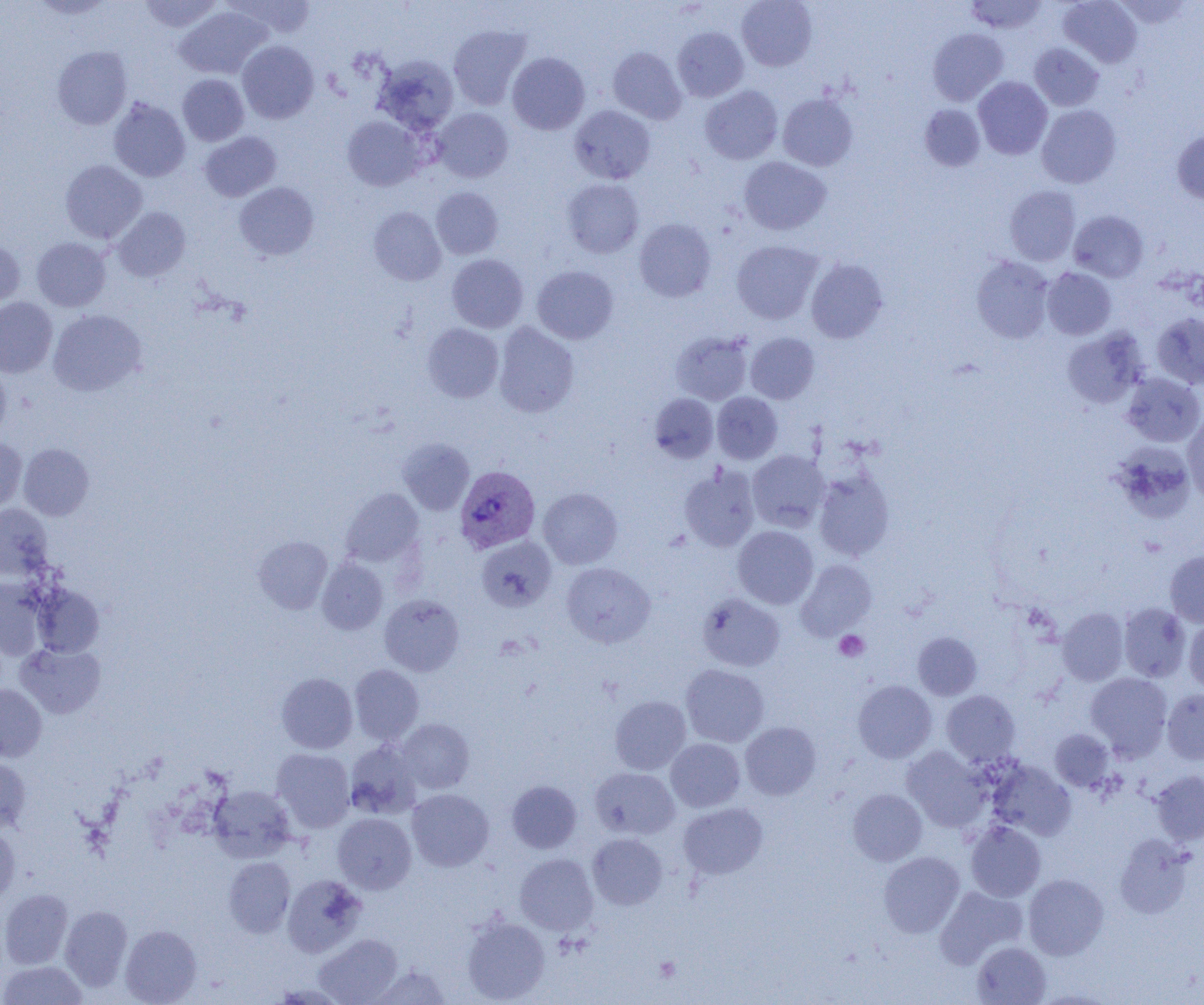
Approximate bounding boxes as [x1, y1, x2, y2] in pixels. Plasmodium vivax-infected red blood cell locations: [455, 466, 540, 553]. Platelet locations: [834, 630, 869, 662], [654, 956, 681, 982]. Uninfected red blood cell locations: [28, 0, 117, 19], [139, 0, 222, 32], [227, 0, 317, 40], [737, 0, 817, 71], [966, 0, 1047, 34], [1059, 0, 1142, 67], [1113, 1, 1194, 29], [176, 6, 270, 79], [448, 25, 531, 110], [672, 27, 749, 101], [927, 28, 1008, 106], [237, 41, 319, 123], [1029, 43, 1104, 111], [52, 46, 132, 130], [608, 47, 686, 124], [507, 52, 590, 135], [374, 55, 458, 135], [177, 74, 249, 146], [973, 77, 1052, 159], [700, 85, 782, 164], [778, 93, 858, 171], [108, 97, 190, 182], [919, 104, 985, 171], [569, 105, 655, 184], [1037, 105, 1121, 188], [433, 108, 513, 182], [342, 116, 424, 190], [1172, 130, 1204, 203], [199, 131, 281, 202], [739, 156, 830, 235], [60, 159, 147, 243], [562, 178, 643, 257], [234, 182, 318, 260], [1004, 185, 1081, 266], [431, 187, 503, 259], [369, 206, 446, 285], [112, 207, 190, 281], [1069, 210, 1149, 282], [634, 218, 716, 302], [32, 238, 111, 311], [0, 240, 25, 308], [732, 240, 823, 324], [447, 254, 528, 332], [971, 256, 1055, 343], [806, 258, 888, 343], [532, 265, 618, 344], [1042, 267, 1117, 340], [0, 297, 57, 377], [48, 309, 146, 396], [1152, 312, 1204, 388], [494, 322, 579, 417], [422, 323, 504, 402], [1062, 328, 1147, 408], [671, 331, 752, 405], [745, 332, 819, 404], [0, 365, 12, 439], [1121, 373, 1203, 447], [712, 392, 782, 464], [649, 393, 718, 462], [1183, 414, 1204, 505], [0, 438, 27, 515], [398, 438, 474, 515], [1109, 442, 1196, 522], [19, 444, 94, 520], [747, 450, 830, 532], [679, 465, 760, 551], [813, 468, 895, 561], [538, 487, 623, 569], [340, 488, 424, 567], [0, 504, 53, 580], [732, 525, 818, 609], [253, 536, 333, 614], [476, 537, 556, 611], [1165, 550, 1204, 626], [317, 558, 388, 634], [796, 559, 876, 639], [562, 562, 655, 647], [0, 577, 47, 660], [32, 584, 104, 657], [697, 593, 785, 671], [379, 594, 463, 676], [1119, 603, 1191, 682], [1057, 607, 1128, 686], [1184, 617, 1204, 693], [913, 632, 982, 700], [16, 643, 105, 718], [350, 664, 424, 744], [680, 664, 769, 747], [276, 673, 357, 753], [1086, 673, 1173, 760], [852, 680, 937, 763], [0, 684, 47, 761], [1162, 689, 1204, 764], [942, 690, 1020, 766], [610, 696, 691, 774], [396, 719, 474, 793], [740, 722, 821, 800], [1050, 728, 1113, 791], [666, 738, 745, 811], [345, 741, 423, 819], [902, 746, 991, 831], [272, 748, 355, 832], [0, 758, 31, 832], [987, 759, 1076, 840], [590, 767, 679, 839], [1151, 770, 1204, 845], [507, 780, 582, 853], [208, 785, 296, 863], [407, 788, 494, 871], [847, 789, 927, 865], [679, 803, 767, 879], [333, 813, 416, 893], [966, 820, 1045, 901], [0, 824, 20, 902], [588, 833, 667, 909], [1115, 834, 1194, 919], [878, 851, 965, 937], [515, 854, 598, 934], [223, 856, 295, 937], [282, 874, 367, 957], [1023, 874, 1109, 959], [936, 886, 1027, 966], [0, 888, 73, 969], [60, 905, 132, 991], [461, 916, 550, 1003], [120, 925, 202, 1004], [313, 933, 402, 1004], [972, 941, 1051, 1004], [0, 960, 87, 1005], [370, 964, 451, 1004]. Slide-level diagnosis: Plasmodium vivax. Light microscopy. One field of a larger specimen. Thin blood smear. 1000x magnification. Image is 1204×1005 pixels.